Give the position of every malaria parasite.
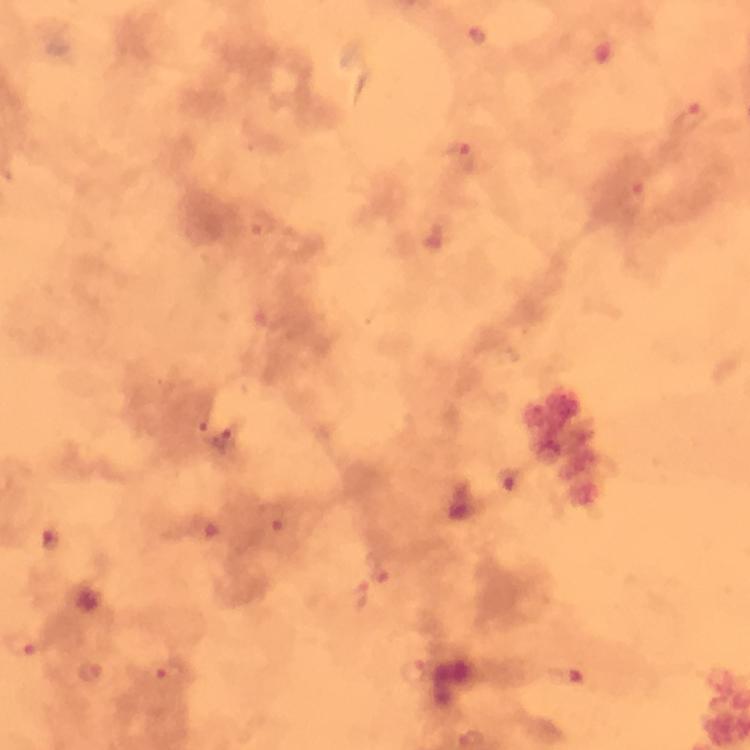

Approximate object centers, in pixels from the top-left corner.
Malaria parasites: (x=479, y=33), (x=689, y=117), (x=461, y=155), (x=633, y=197), (x=264, y=224), (x=198, y=421), (x=230, y=439), (x=509, y=481), (x=272, y=517), (x=381, y=567), (x=22, y=643), (x=91, y=671), (x=413, y=672), (x=171, y=676), (x=567, y=676).

image_size: 750×750 pixels
capture: smartphone camera through the microscope
context: from a diagnostic examination for malaria
stain: Giemsa
cropped_from: one field of view
magnification: 100x
preparation: thick blood smear
immersion_oil: applied